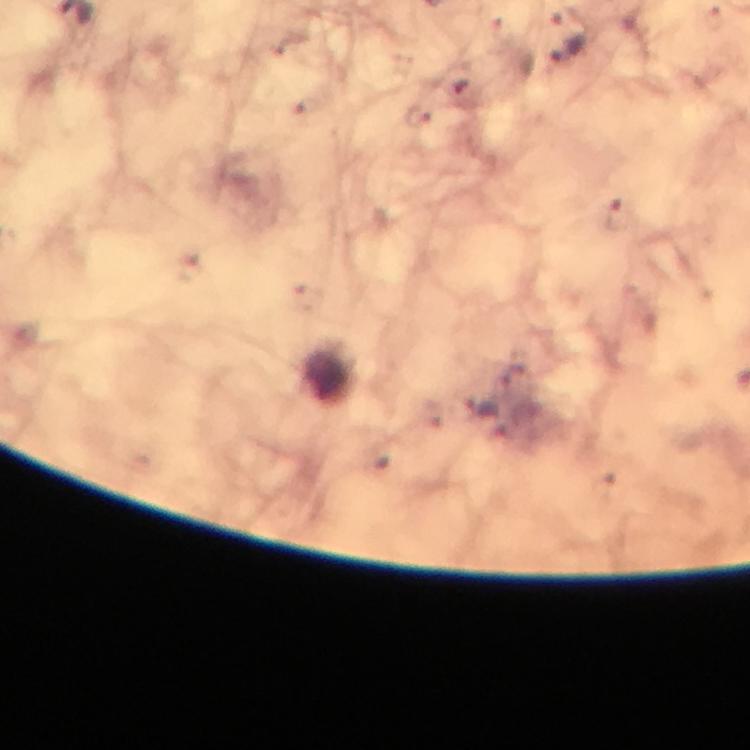

capture: smartphone camera through the microscope
malaria_parasite_locations: 'approximate object centers, in pixels from the top-left corner: (x=418, y=116), (x=617, y=216)'
context: from a diagnostic examination for malaria
stain: Giemsa
image_size: 750×750 pixels
cropped_from: a single field of view
preparation: thick smear
magnification: 100x
immersion_oil: applied